Identify the preparation type.
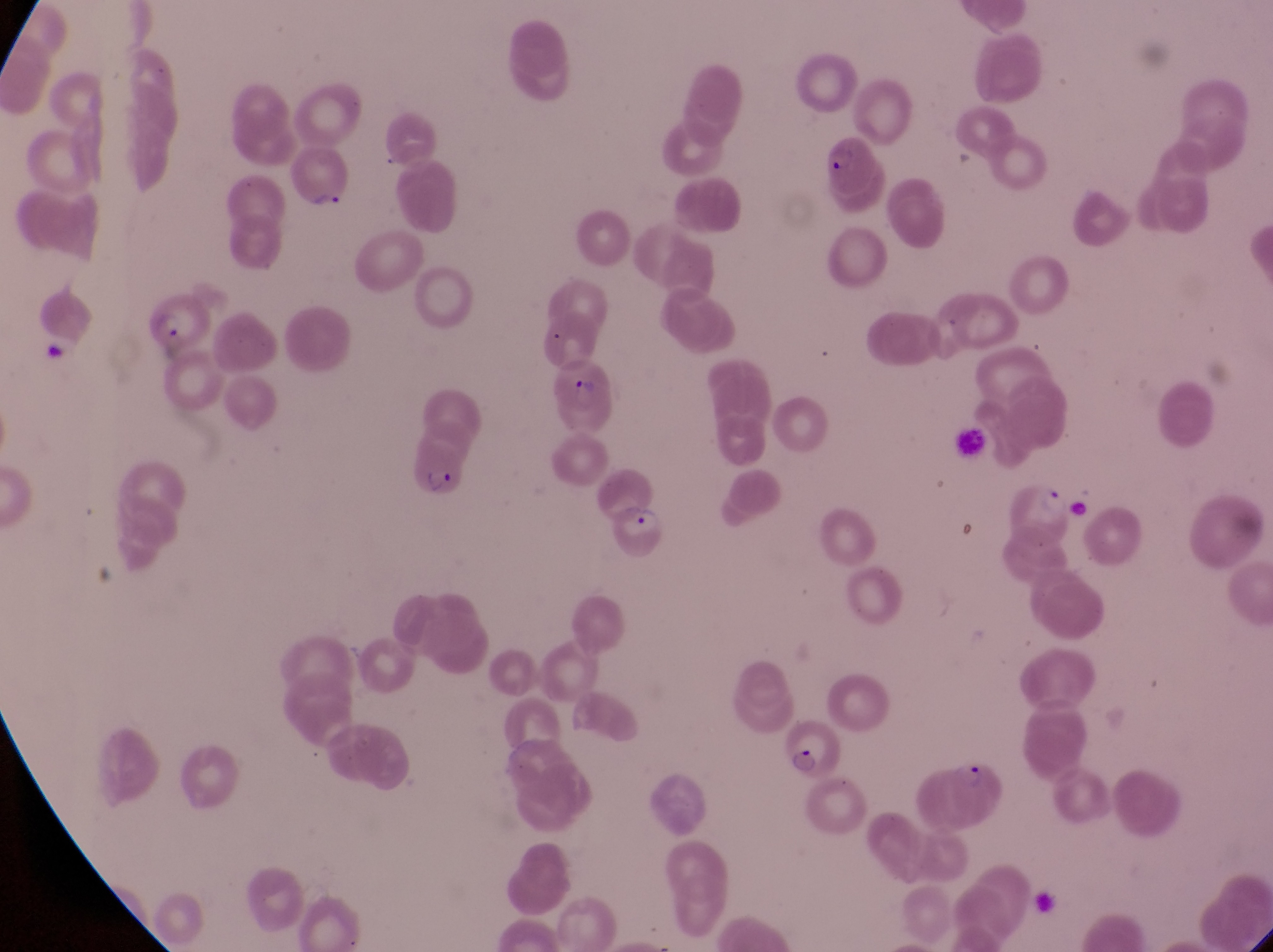
This is a thin smear.

Approximate bounding boxes as left top right bottom in pixels. Parasitised red blood cell locations: 811 132 880 197; 290 150 353 215; 145 292 215 355; 552 362 614 436; 402 434 457 499; 993 475 1080 549; 616 504 669 562; 781 719 841 777; 948 757 1015 829. Artifact (platelet-like body, stain precipitate, or debris) locations: 40 334 70 366. Photographed through the eyepiece of an Olympus CX-23 microscope with a smartphone camera. Sample from Uganda. At a magnification of 1000x. Single field of view. Image is 1273×952 pixels.